Give the position of every leukocyte visible.
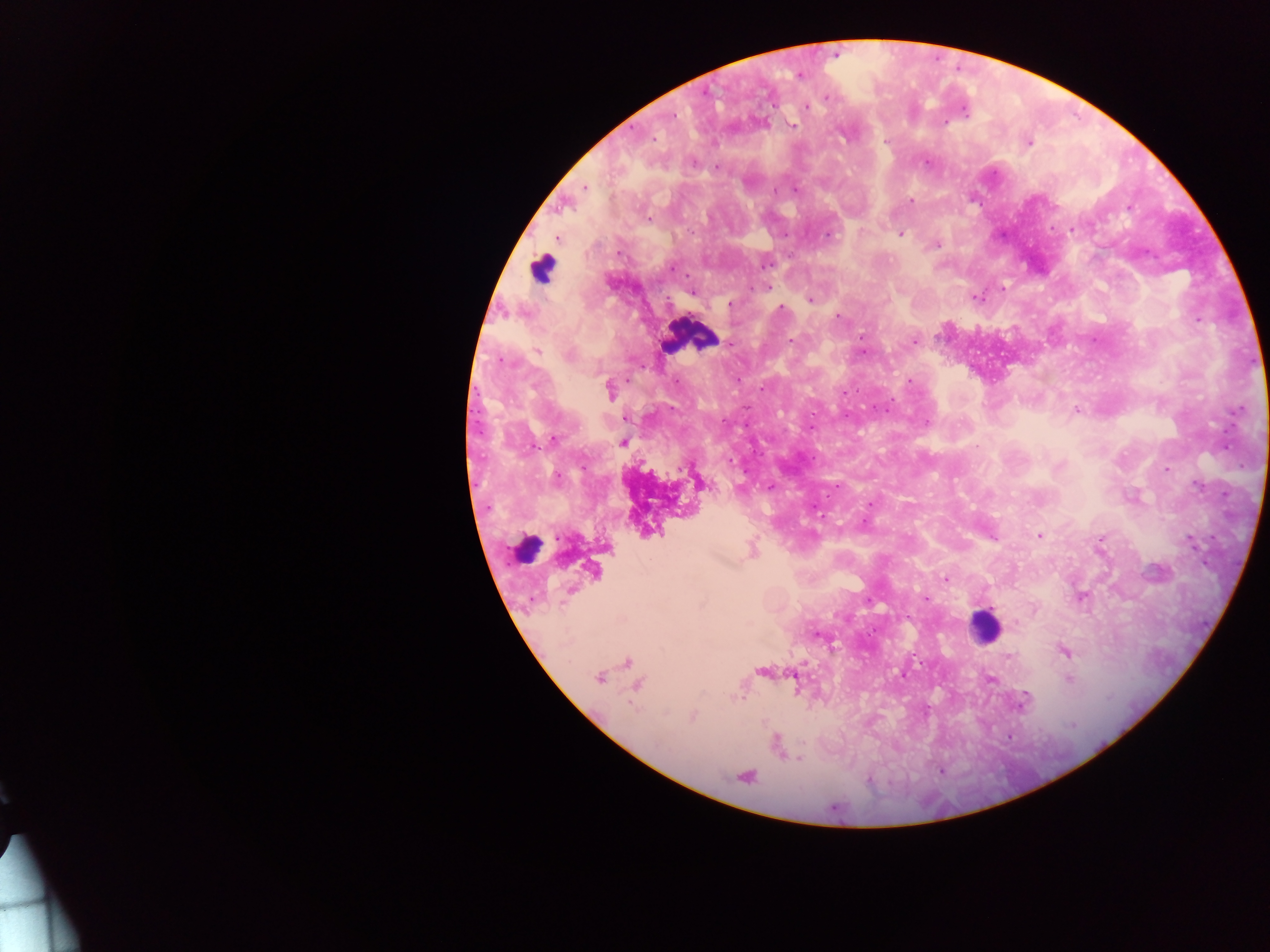

Approximate centers as {x, y} in pixels.
Leukocytes: {542, 271}, {691, 335}, {523, 548}, {985, 625}.

Plasmodium parasite locations: {800, 76}, {826, 97}, {806, 107}, {965, 112}, {673, 116}, {945, 122}, {792, 125}, {655, 139}, {884, 142}, {1029, 143}, {694, 163}, {716, 167}, {585, 187}, {775, 190}, {796, 190}, {911, 201}, {1129, 207}, {648, 220}, {1071, 230}, {785, 235}, {902, 235}, {827, 236}, {557, 239}, {937, 246}, {765, 264}, {671, 268}, {767, 287}, {1003, 288}, {692, 293}, {976, 298}, {809, 300}, {729, 304}, {780, 308}, {837, 316}, {1197, 321}, {862, 337}, {792, 340}, {914, 342}, {538, 350}, {863, 353}, {568, 355}, {909, 381}, {677, 382}, {761, 389}, {610, 390}, {886, 410}, {1076, 411}, {927, 422}, {555, 438}, {623, 443}, {729, 461}, {1059, 466}, {1167, 469}, {557, 477}, {1198, 486}, {770, 487}, {871, 504}, {864, 522}, {1040, 536}, {993, 537}, {1101, 538}, {1192, 542}, {945, 579}, {925, 599}, {869, 601}, {817, 635}, {1064, 651}, {1007, 657}, {805, 663}, {904, 676}, {599, 678}, {991, 679}, {1069, 679}, {741, 698}, {1022, 703}, {693, 717}, {1072, 724}, {775, 743}, {799, 759}, {939, 771}, {869, 780}. Collected in Ghana. Photographed through a microscope with a mobile-phone camera. Thick blood smear. Image is 1270×952 pixels. Single field of view.